Comment on the morphology of the red blood cells.
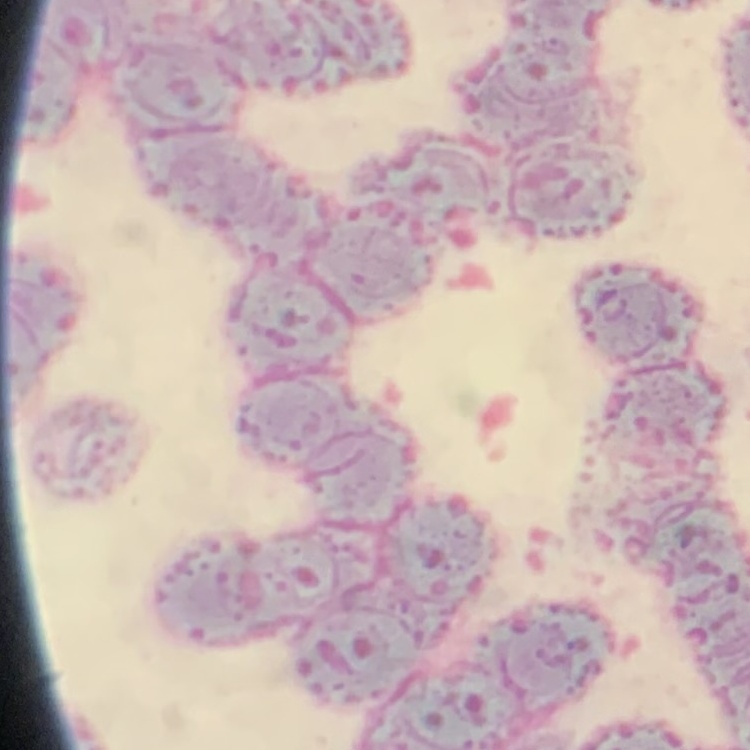

They show rouleaux formation.

stain = Field's or Giemsa
preparation = thin blood film
image type = square crop of a larger photomicrograph